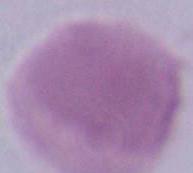

magnification: 1000x
identification: red blood cell
modality: micrograph